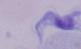 Photomicrograph. Captured at 1000x magnification. A trypanosome is shown.